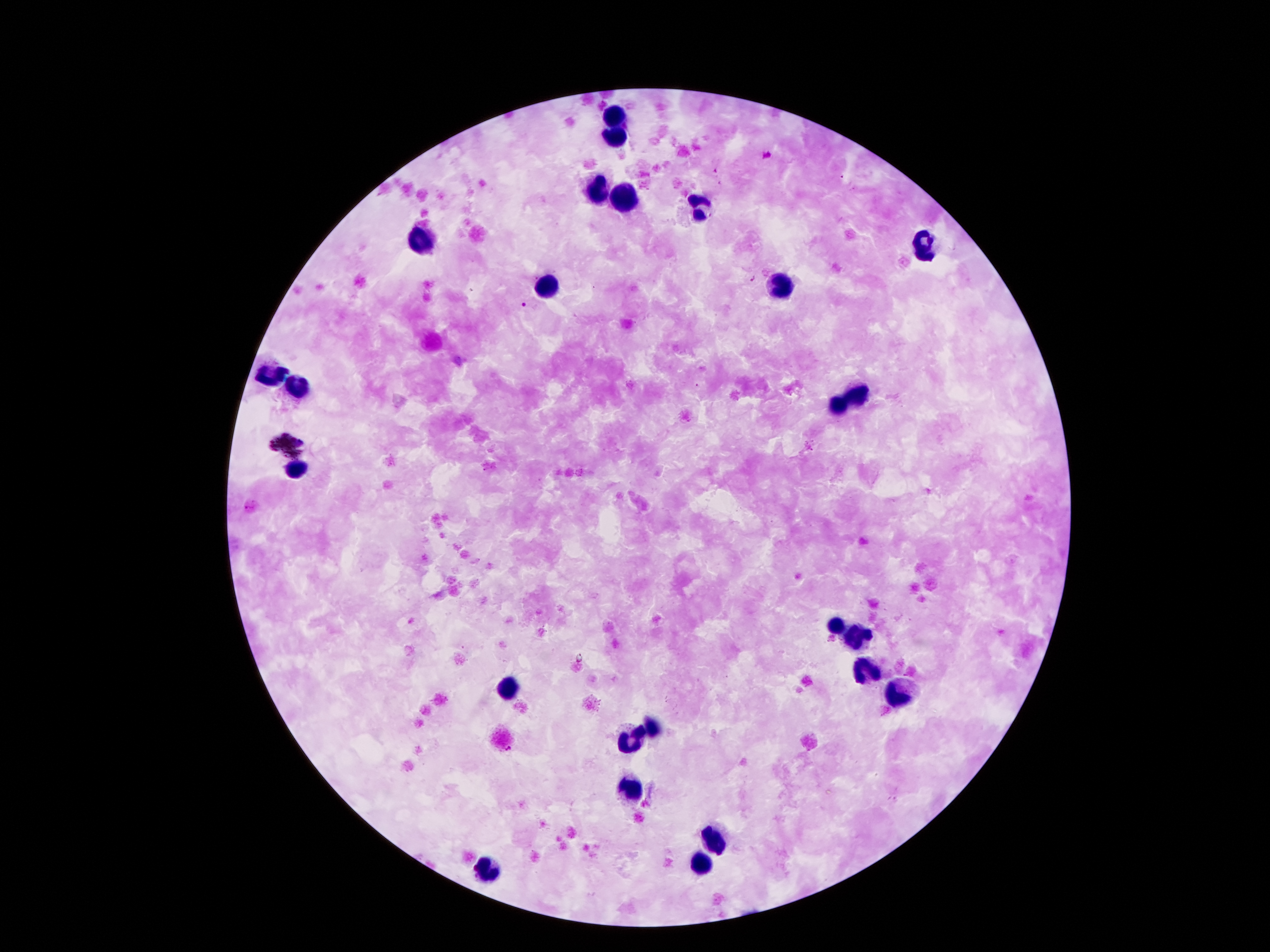 Approximate object centers, in pixels from the top-left corner. Leukocyte locations: (x=615, y=117), (x=611, y=137), (x=595, y=191), (x=621, y=193), (x=701, y=209), (x=423, y=241), (x=923, y=247), (x=781, y=283), (x=545, y=289), (x=267, y=377), (x=295, y=385), (x=857, y=393), (x=837, y=405), (x=299, y=471), (x=837, y=627), (x=857, y=639), (x=865, y=667), (x=509, y=689), (x=897, y=697), (x=651, y=727), (x=631, y=743), (x=629, y=787), (x=715, y=839), (x=699, y=863), (x=489, y=869). Plasmodium parasite locations: (x=765, y=154), (x=715, y=172), (x=843, y=178), (x=752, y=279), (x=524, y=305), (x=697, y=386). Patient malaria status: infected with Plasmodium falciparum. Thick peripheral-blood smear. Smartphone photograph taken through the microscope eyepiece. Image is 1270×952 pixels. Single field of view. Giemsa-stained preparation. 100x magnification.